Classify this cell by malaria status.
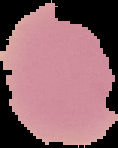

It is uninfected.

image size = 118×148 pixels
preparation = thin blood smear
image type = cell region segmented out of the field of view; surrounding area masked to black